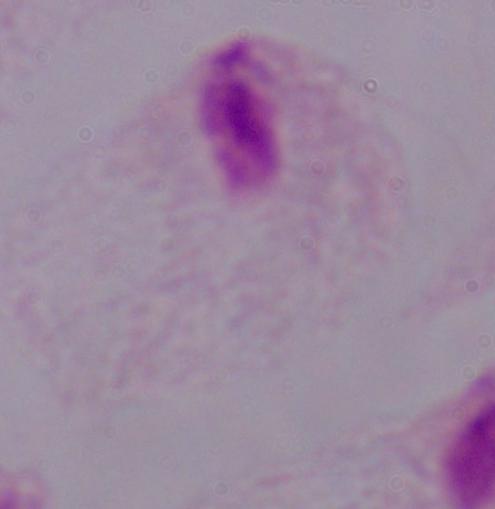
A trichomonad is seen. Photomicrograph. Captured at 1000x magnification.